Classify this cell by malaria status.
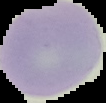
It is uninfected.

Summary:
  - Preparation: thin blood smear
  - Image type: segmented cell region on a black background
  - Image size: 106×103 pixels